Outline each Plasmodium vivax-infected red blood cell.
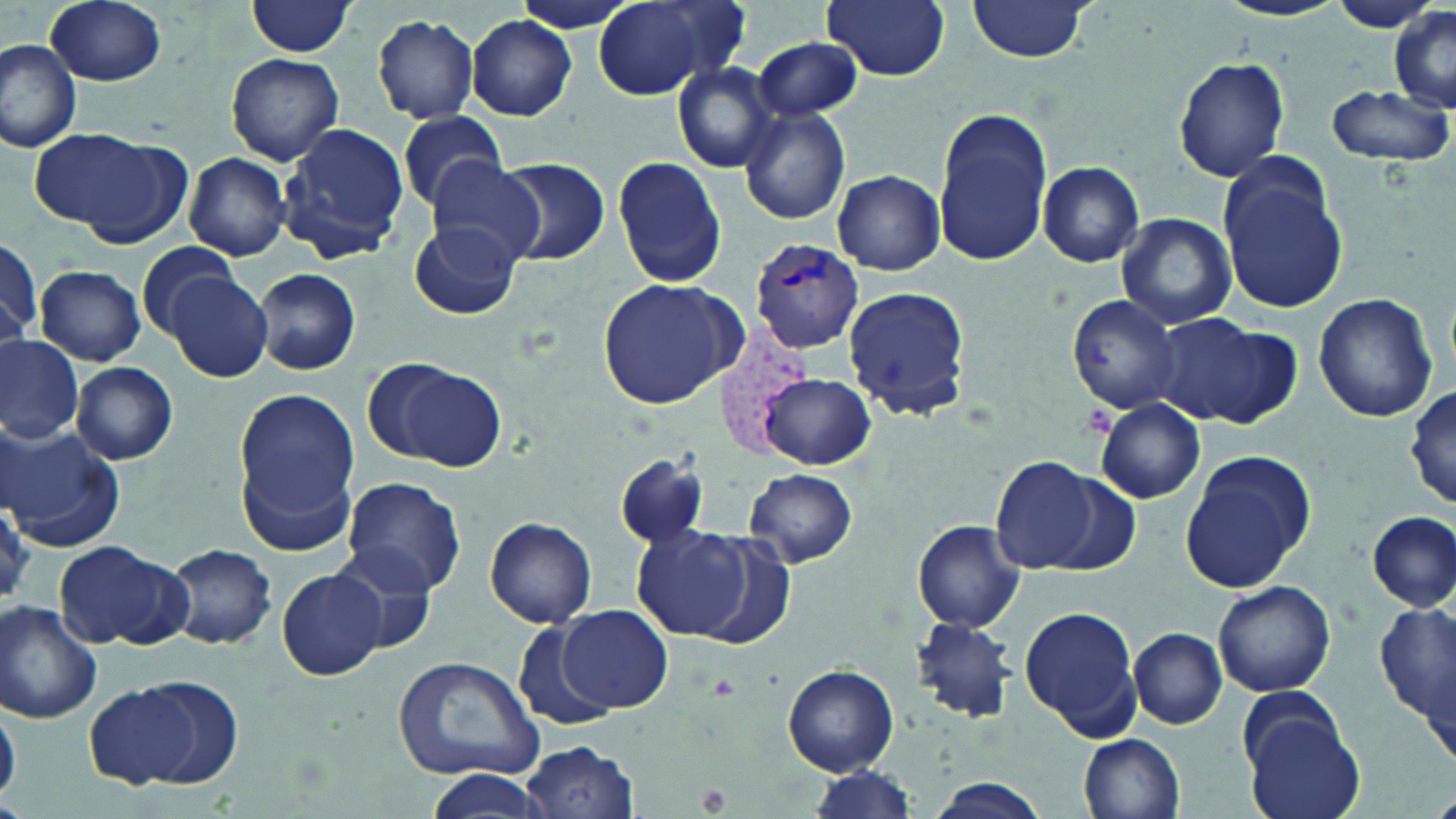

Approximate bounding boxes as named x1/y1/x2/y2 corners in pixels.
Plasmodium vivax-infected red blood cells: (x1=751, y1=237, x2=866, y2=352).

slide-level diagnosis = Plasmodium vivax
modality = optical microscopy
preparation = thin blood smear
uninfected red blood cell locations = approximate bounding boxes as named x1/y1/x2/y2 corners in pixels: (x1=46, y1=0, x2=168, y2=86), (x1=821, y1=0, x2=951, y2=81), (x1=965, y1=0, x2=1093, y2=62), (x1=1327, y1=0, x2=1442, y2=33), (x1=594, y1=1, x2=742, y2=99), (x1=1214, y1=1, x2=1347, y2=23), (x1=245, y1=2, x2=359, y2=57), (x1=1390, y1=7, x2=1456, y2=113), (x1=371, y1=13, x2=480, y2=124), (x1=466, y1=15, x2=578, y2=120), (x1=752, y1=34, x2=864, y2=123), (x1=0, y1=38, x2=82, y2=153), (x1=225, y1=53, x2=344, y2=166), (x1=1173, y1=56, x2=1291, y2=182), (x1=667, y1=61, x2=781, y2=173), (x1=1323, y1=82, x2=1453, y2=169), (x1=738, y1=107, x2=851, y2=225), (x1=932, y1=107, x2=1055, y2=266), (x1=392, y1=113, x2=512, y2=211), (x1=281, y1=123, x2=408, y2=262), (x1=29, y1=126, x2=162, y2=234), (x1=184, y1=152, x2=293, y2=261), (x1=613, y1=154, x2=728, y2=288), (x1=421, y1=155, x2=549, y2=268), (x1=493, y1=155, x2=611, y2=266), (x1=1216, y1=157, x2=1349, y2=317), (x1=1039, y1=161, x2=1143, y2=268), (x1=832, y1=170, x2=945, y2=275), (x1=1115, y1=212, x2=1237, y2=331), (x1=408, y1=219, x2=521, y2=321), (x1=1, y1=237, x2=41, y2=342), (x1=136, y1=240, x2=244, y2=341), (x1=35, y1=265, x2=146, y2=366), (x1=253, y1=267, x2=361, y2=377), (x1=165, y1=272, x2=273, y2=381), (x1=596, y1=277, x2=743, y2=409), (x1=843, y1=284, x2=971, y2=419), (x1=1314, y1=292, x2=1439, y2=424), (x1=1066, y1=294, x2=1180, y2=414), (x1=1152, y1=313, x2=1296, y2=430), (x1=0, y1=336, x2=82, y2=442), (x1=365, y1=358, x2=508, y2=473), (x1=72, y1=362, x2=178, y2=464), (x1=760, y1=373, x2=874, y2=469), (x1=1408, y1=383, x2=1456, y2=513), (x1=232, y1=386, x2=364, y2=541), (x1=1095, y1=399, x2=1206, y2=503), (x1=0, y1=426, x2=122, y2=548), (x1=1177, y1=450, x2=1316, y2=594), (x1=613, y1=452, x2=709, y2=551), (x1=989, y1=455, x2=1110, y2=574), (x1=742, y1=469, x2=860, y2=568), (x1=341, y1=477, x2=467, y2=596), (x1=1366, y1=510, x2=1455, y2=611), (x1=486, y1=516, x2=597, y2=628), (x1=912, y1=519, x2=1027, y2=632), (x1=629, y1=526, x2=756, y2=641), (x1=681, y1=531, x2=798, y2=652), (x1=52, y1=542, x2=184, y2=649), (x1=163, y1=543, x2=278, y2=650), (x1=326, y1=546, x2=440, y2=655), (x1=278, y1=568, x2=388, y2=681), (x1=1211, y1=580, x2=1336, y2=698), (x1=1375, y1=599, x2=1455, y2=732), (x1=0, y1=601, x2=102, y2=723), (x1=1018, y1=603, x2=1143, y2=738), (x1=557, y1=606, x2=672, y2=715), (x1=910, y1=615, x2=1017, y2=724), (x1=513, y1=616, x2=621, y2=730), (x1=1129, y1=626, x2=1227, y2=729), (x1=392, y1=656, x2=547, y2=781), (x1=783, y1=665, x2=898, y2=776), (x1=130, y1=676, x2=244, y2=787), (x1=84, y1=682, x2=202, y2=789), (x1=1238, y1=703, x2=1363, y2=819), (x1=0, y1=704, x2=22, y2=801), (x1=1078, y1=733, x2=1184, y2=819), (x1=522, y1=740, x2=638, y2=819), (x1=801, y1=767, x2=920, y2=819), (x1=422, y1=770, x2=549, y2=819), (x1=925, y1=779, x2=1055, y2=818)
field of view = single
stain = May-Grünwald-Giemsa
magnification = 1000x
image size = 1456×819 pixels